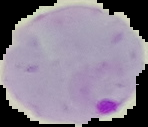
Summary:
  - Image size: 148×127 pixels
  - Preparation: thin blood smear
  - Result: Plasmodium parasites detected
  - Image type: segmented cell region with the area outside set to black